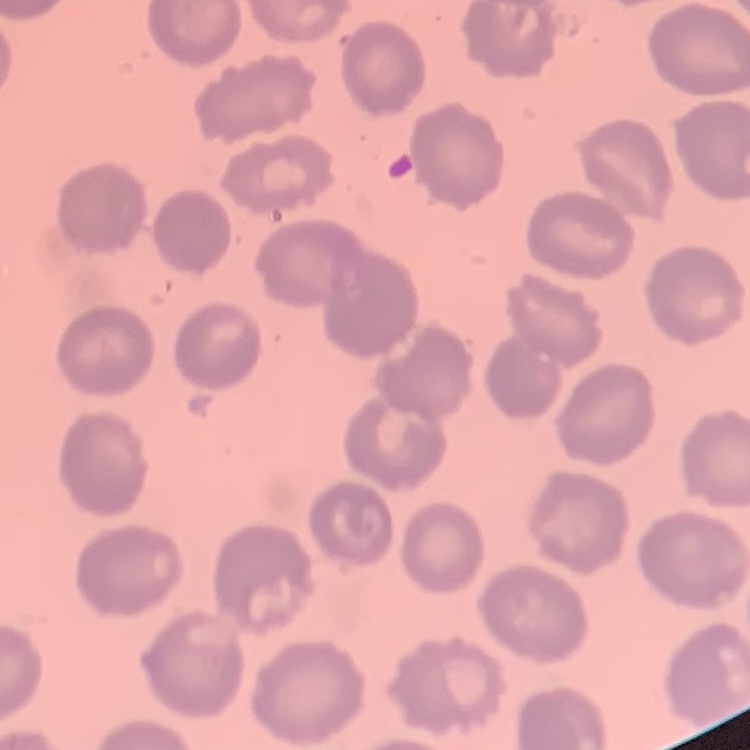
The erythrocytes show no rouleaux formation. Field's or Giemsa stain. Thin peripheral smear. One tile cut from a larger photomicrograph.